Find each white blood cell.
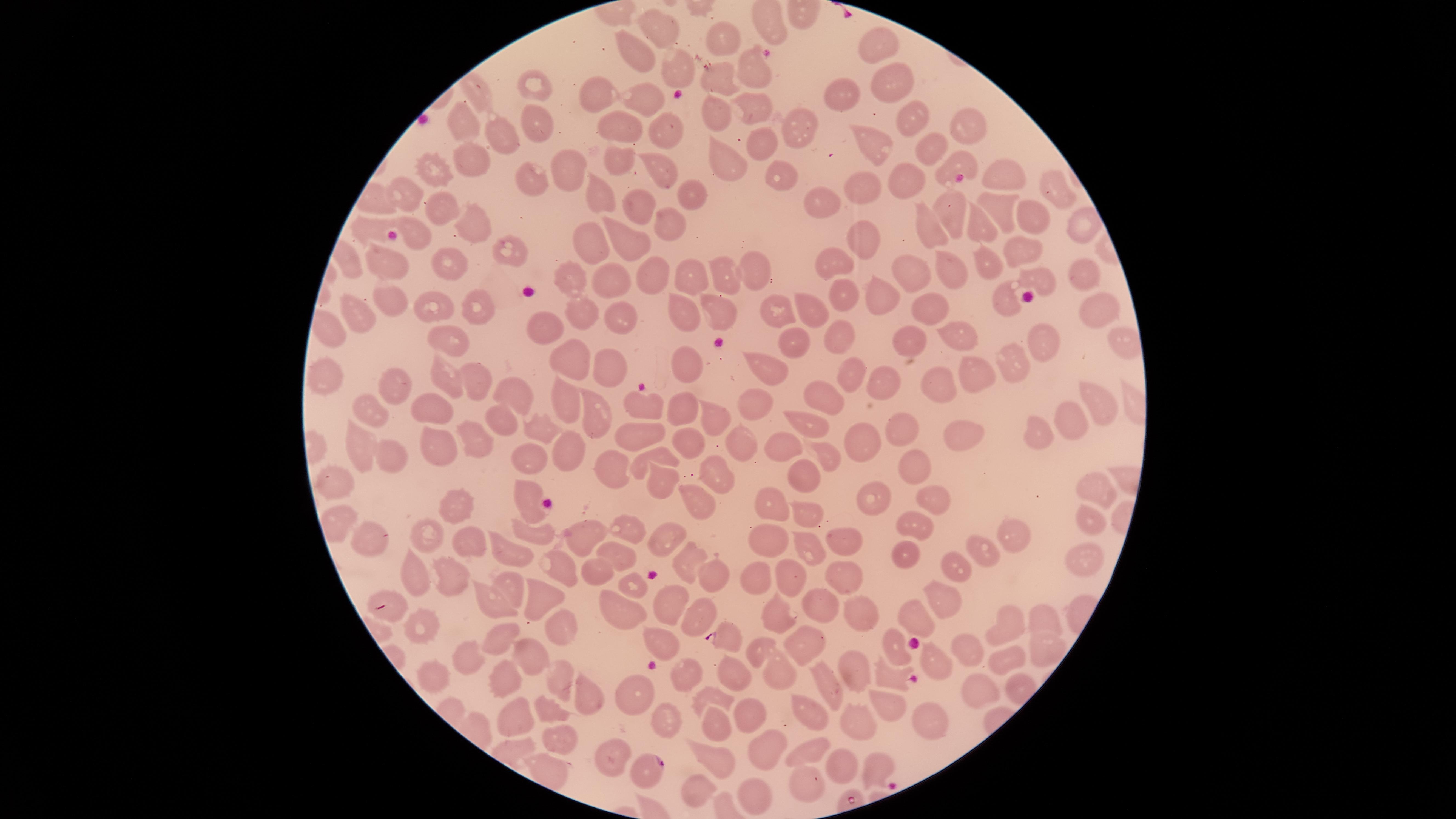
No white blood cells identified.

{
  "visible_region": "circular",
  "parasitized_red_blood_cells": "approximate marker points as (x, y) in pixels: (389, 606), (727, 638), (650, 767)",
  "uninfected_red_blood_cells": "approximate marker points as (x, y) in pixels: (657, 27), (727, 42), (875, 42), (635, 54), (679, 69), (754, 70), (717, 76), (889, 79), (536, 89), (592, 97), (846, 98), (645, 100), (754, 104), (713, 109), (537, 118), (910, 120), (801, 124), (963, 124), (663, 125), (467, 127), (627, 129), (504, 137), (873, 145), (763, 146), (930, 148), (618, 156), (468, 157), (718, 157), (953, 163), (567, 165), (661, 168), (436, 172), (997, 174), (778, 179), (536, 180), (902, 182), (692, 188), (1054, 188), (870, 191), (407, 196), (601, 196), (824, 203), (438, 208), (640, 208), (947, 211), (1002, 212), (1036, 218), (672, 221), (473, 224), (367, 227), (980, 227), (1084, 228), (930, 230), (413, 235), (865, 236), (1020, 240), (592, 242), (622, 242), (510, 250), (450, 259), (985, 259), (387, 263), (837, 263), (952, 264), (756, 269), (650, 273), (691, 273), (727, 275), (914, 275), (1084, 275), (571, 280), (610, 280), (1039, 280), (878, 292), (385, 296), (837, 298), (476, 302), (1006, 302), (928, 304), (435, 307), (1091, 308), (809, 309), (777, 310), (685, 311), (358, 312), (586, 312), (723, 313), (629, 320), (328, 328), (957, 328), (546, 333), (837, 334), (1048, 337), (449, 339), (910, 339), (798, 340), (1009, 358), (569, 362), (685, 362), (610, 364), (765, 370), (984, 370), (323, 371), (850, 372), (880, 377), (445, 378), (473, 382), (939, 384), (398, 385), (509, 392), (822, 395), (1096, 398), (759, 399), (565, 401), (645, 405), (431, 407), (682, 408), (589, 409), (710, 411), (375, 413), (498, 418), (1075, 420), (805, 425), (1044, 431), (542, 432), (644, 432), (911, 432), (468, 438), (964, 438), (692, 440), (735, 441), (867, 442), (358, 443), (435, 444), (784, 445), (566, 448), (656, 454), (829, 455), (530, 457), (390, 459), (905, 465), (616, 470), (716, 473), (802, 475), (658, 478), (332, 480), (1099, 488), (526, 493), (924, 497), (876, 498), (693, 501), (775, 502), (455, 504), (801, 512), (1089, 518), (522, 524), (917, 526), (629, 531), (590, 535), (1011, 535), (377, 536), (840, 536), (659, 537), (772, 539), (471, 540), (430, 541), (801, 544), (902, 550), (512, 552), (616, 554), (690, 555), (983, 555), (1084, 559), (558, 561), (841, 571), (954, 571), (595, 572), (790, 574), (410, 576), (448, 576), (758, 576), (718, 577), (512, 582), (628, 584), (941, 593), (542, 598), (674, 602), (820, 603), (492, 604), (624, 609), (859, 612), (700, 616), (917, 616), (775, 618), (1010, 621), (1044, 621), (555, 627), (425, 631), (495, 637), (658, 637), (801, 638), (757, 652), (895, 652), (1044, 653), (969, 654), (528, 655), (475, 656), (1005, 659), (931, 665), (852, 668), (727, 672), (683, 674), (775, 675), (430, 676), (828, 676), (891, 678), (497, 679), (559, 680), (982, 680), (584, 695), (631, 696), (717, 696), (889, 706), (804, 710), (552, 713), (747, 714), (663, 716), (512, 719), (860, 722), (934, 722), (717, 724), (563, 738), (764, 748), (813, 748), (617, 757), (711, 762), (841, 764), (545, 767), (876, 770), (808, 780), (688, 791), (747, 797)",
  "preparation": "thin blood smear",
  "presence": "malaria parasites detected",
  "species": "Plasmodium falciparum",
  "field_of_view": "single",
  "capture": "smartphone photograph through the microscope eyepiece",
  "image_size": "1456×819 pixels",
  "stain": "Giemsa"
}